State the blood parasite species.
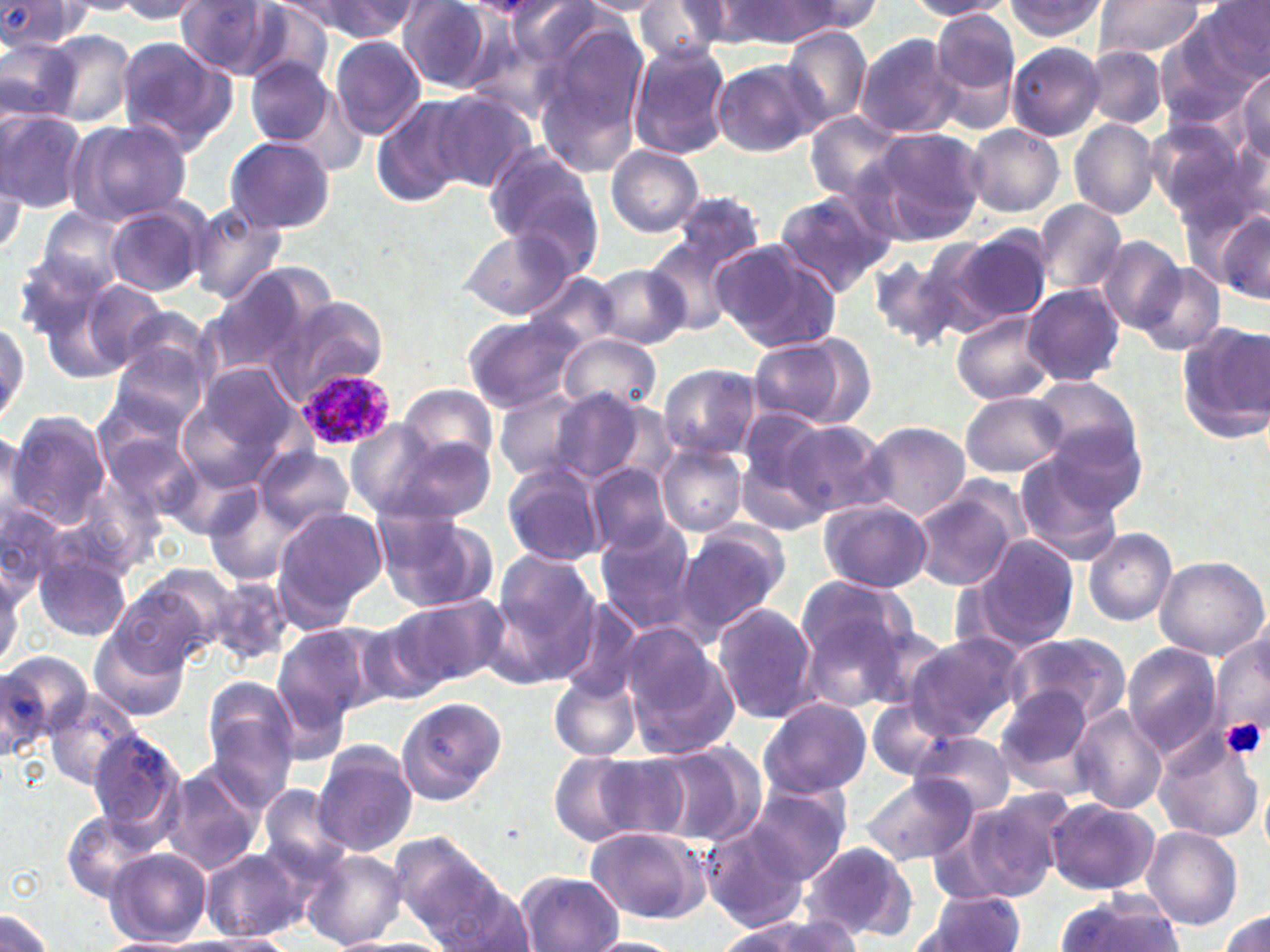
Plasmodium ovale.

{
  "modality": "optical microscopy",
  "preparation": "thin blood smear",
  "uninfected_red_blood_cell_locations": "approximate bounding boxes as named x1/y1/x2/y2 corners in pixels: (x1=174, y1=0, x2=284, y2=77), (x1=310, y1=0, x2=420, y2=43), (x1=503, y1=0, x2=602, y2=70), (x1=575, y1=0, x2=670, y2=15), (x1=782, y1=0, x2=883, y2=36), (x1=908, y1=0, x2=1014, y2=19), (x1=1094, y1=0, x2=1208, y2=60), (x1=1197, y1=0, x2=1269, y2=86), (x1=109, y1=1, x2=207, y2=22), (x1=398, y1=1, x2=496, y2=91), (x1=723, y1=1, x2=838, y2=46), (x1=1004, y1=1, x2=1109, y2=44), (x1=1, y1=2, x2=90, y2=69), (x1=633, y1=2, x2=725, y2=64), (x1=228, y1=3, x2=333, y2=83), (x1=932, y1=11, x2=1021, y2=109), (x1=532, y1=22, x2=648, y2=177), (x1=780, y1=28, x2=872, y2=126), (x1=1154, y1=28, x2=1252, y2=130), (x1=45, y1=29, x2=136, y2=127), (x1=856, y1=33, x2=962, y2=140), (x1=114, y1=35, x2=236, y2=155), (x1=329, y1=35, x2=426, y2=141), (x1=0, y1=36, x2=80, y2=125), (x1=1006, y1=40, x2=1104, y2=141), (x1=629, y1=45, x2=733, y2=160), (x1=1085, y1=46, x2=1167, y2=128), (x1=246, y1=58, x2=337, y2=146), (x1=711, y1=58, x2=821, y2=157), (x1=1235, y1=68, x2=1269, y2=162), (x1=426, y1=90, x2=537, y2=194), (x1=371, y1=96, x2=472, y2=206), (x1=0, y1=108, x2=87, y2=214), (x1=805, y1=112, x2=905, y2=201), (x1=1143, y1=117, x2=1256, y2=232), (x1=63, y1=118, x2=195, y2=228), (x1=1070, y1=118, x2=1160, y2=219), (x1=965, y1=123, x2=1064, y2=216), (x1=862, y1=126, x2=988, y2=240), (x1=224, y1=136, x2=336, y2=234), (x1=606, y1=146, x2=705, y2=237), (x1=486, y1=150, x2=604, y2=268), (x1=0, y1=160, x2=28, y2=264), (x1=772, y1=188, x2=898, y2=296), (x1=665, y1=190, x2=767, y2=274), (x1=1033, y1=198, x2=1126, y2=297), (x1=103, y1=200, x2=211, y2=296), (x1=189, y1=201, x2=288, y2=308), (x1=1211, y1=206, x2=1270, y2=305), (x1=35, y1=207, x2=130, y2=296), (x1=459, y1=228, x2=576, y2=320), (x1=950, y1=229, x2=1051, y2=328), (x1=645, y1=236, x2=748, y2=335), (x1=1096, y1=236, x2=1185, y2=332), (x1=713, y1=240, x2=841, y2=354), (x1=11, y1=252, x2=111, y2=349), (x1=867, y1=252, x2=965, y2=351), (x1=1132, y1=262, x2=1226, y2=356), (x1=593, y1=263, x2=691, y2=351), (x1=202, y1=271, x2=316, y2=375), (x1=527, y1=271, x2=620, y2=355), (x1=67, y1=272, x2=174, y2=376), (x1=1021, y1=284, x2=1124, y2=387), (x1=278, y1=295, x2=390, y2=401), (x1=110, y1=303, x2=217, y2=394), (x1=951, y1=311, x2=1055, y2=406), (x1=0, y1=316, x2=30, y2=427), (x1=462, y1=316, x2=581, y2=413), (x1=1177, y1=319, x2=1270, y2=443), (x1=559, y1=333, x2=661, y2=415), (x1=747, y1=333, x2=871, y2=429), (x1=104, y1=342, x2=207, y2=439), (x1=659, y1=364, x2=760, y2=459), (x1=182, y1=370, x2=293, y2=490), (x1=1028, y1=376, x2=1147, y2=477), (x1=398, y1=384, x2=499, y2=470), (x1=495, y1=387, x2=592, y2=483), (x1=544, y1=390, x2=657, y2=487), (x1=961, y1=391, x2=1067, y2=479), (x1=735, y1=410, x2=834, y2=522), (x1=5, y1=412, x2=112, y2=530), (x1=782, y1=419, x2=890, y2=519), (x1=345, y1=421, x2=442, y2=517), (x1=857, y1=421, x2=971, y2=521), (x1=0, y1=425, x2=27, y2=525), (x1=372, y1=433, x2=494, y2=525), (x1=657, y1=445, x2=748, y2=537), (x1=256, y1=446, x2=354, y2=533), (x1=1014, y1=449, x2=1128, y2=565), (x1=502, y1=463, x2=610, y2=566), (x1=587, y1=463, x2=677, y2=556), (x1=204, y1=485, x2=317, y2=588), (x1=911, y1=488, x2=1021, y2=590), (x1=0, y1=500, x2=70, y2=604), (x1=818, y1=500, x2=932, y2=593), (x1=272, y1=506, x2=386, y2=621), (x1=371, y1=506, x2=497, y2=615), (x1=594, y1=523, x2=697, y2=633), (x1=675, y1=523, x2=788, y2=638), (x1=1083, y1=528, x2=1178, y2=626), (x1=961, y1=536, x2=1081, y2=656), (x1=32, y1=549, x2=132, y2=643), (x1=487, y1=552, x2=602, y2=682), (x1=1153, y1=554, x2=1270, y2=660), (x1=113, y1=566, x2=235, y2=673), (x1=794, y1=574, x2=918, y2=668), (x1=209, y1=575, x2=293, y2=666), (x1=394, y1=593, x2=507, y2=690), (x1=551, y1=597, x2=647, y2=705), (x1=712, y1=603, x2=820, y2=723), (x1=799, y1=611, x2=910, y2=713), (x1=357, y1=615, x2=451, y2=708), (x1=271, y1=623, x2=388, y2=730), (x1=621, y1=626, x2=739, y2=757), (x1=1209, y1=626, x2=1268, y2=757), (x1=87, y1=629, x2=189, y2=723), (x1=904, y1=632, x2=1024, y2=741), (x1=1001, y1=632, x2=1129, y2=729), (x1=1122, y1=644, x2=1223, y2=759), (x1=0, y1=658, x2=55, y2=764), (x1=548, y1=672, x2=642, y2=763), (x1=199, y1=678, x2=300, y2=799), (x1=993, y1=688, x2=1100, y2=796), (x1=42, y1=690, x2=140, y2=791), (x1=395, y1=696, x2=507, y2=804), (x1=758, y1=696, x2=871, y2=800), (x1=867, y1=700, x2=956, y2=780), (x1=1069, y1=705, x2=1168, y2=814), (x1=1153, y1=729, x2=1263, y2=842), (x1=87, y1=730, x2=184, y2=835), (x1=911, y1=730, x2=1016, y2=815), (x1=653, y1=742, x2=767, y2=845), (x1=312, y1=744, x2=418, y2=857), (x1=547, y1=752, x2=648, y2=848), (x1=593, y1=753, x2=695, y2=842), (x1=159, y1=765, x2=266, y2=875), (x1=861, y1=773, x2=979, y2=867), (x1=746, y1=783, x2=853, y2=884), (x1=255, y1=785, x2=354, y2=891), (x1=963, y1=788, x2=1076, y2=900), (x1=1045, y1=798, x2=1158, y2=894), (x1=61, y1=811, x2=162, y2=903), (x1=701, y1=821, x2=810, y2=931), (x1=585, y1=825, x2=711, y2=925), (x1=1140, y1=826, x2=1243, y2=930), (x1=799, y1=839, x2=917, y2=942), (x1=106, y1=847, x2=212, y2=946), (x1=201, y1=848, x2=305, y2=942), (x1=302, y1=849, x2=407, y2=950), (x1=401, y1=850, x2=527, y2=949), (x1=517, y1=870, x2=623, y2=951), (x1=913, y1=890, x2=1027, y2=951), (x1=1054, y1=893, x2=1185, y2=952), (x1=0, y1=909, x2=53, y2=949), (x1=1215, y1=910, x2=1270, y2=951), (x1=717, y1=915, x2=859, y2=952), (x1=192, y1=933, x2=296, y2=952), (x1=95, y1=936, x2=203, y2=952), (x1=347, y1=937, x2=458, y2=952), (x1=585, y1=937, x2=686, y2=952)",
  "field_of_view": "single",
  "magnification": "1000x",
  "image_size": "1270×952 pixels",
  "stain": "May-Grünwald-Giemsa",
  "platelet_locations": "approximate bounding boxes as named x1/y1/x2/y2 corners in pixels: (x1=1222, y1=717, x2=1266, y2=761)",
  "plasmodium_ovale_infected_red_blood_cell_locations": "approximate bounding boxes as named x1/y1/x2/y2 corners in pixels: (x1=292, y1=365, x2=394, y2=452)"
}